Locate every Plasmodium malariae-infected red blood cell.
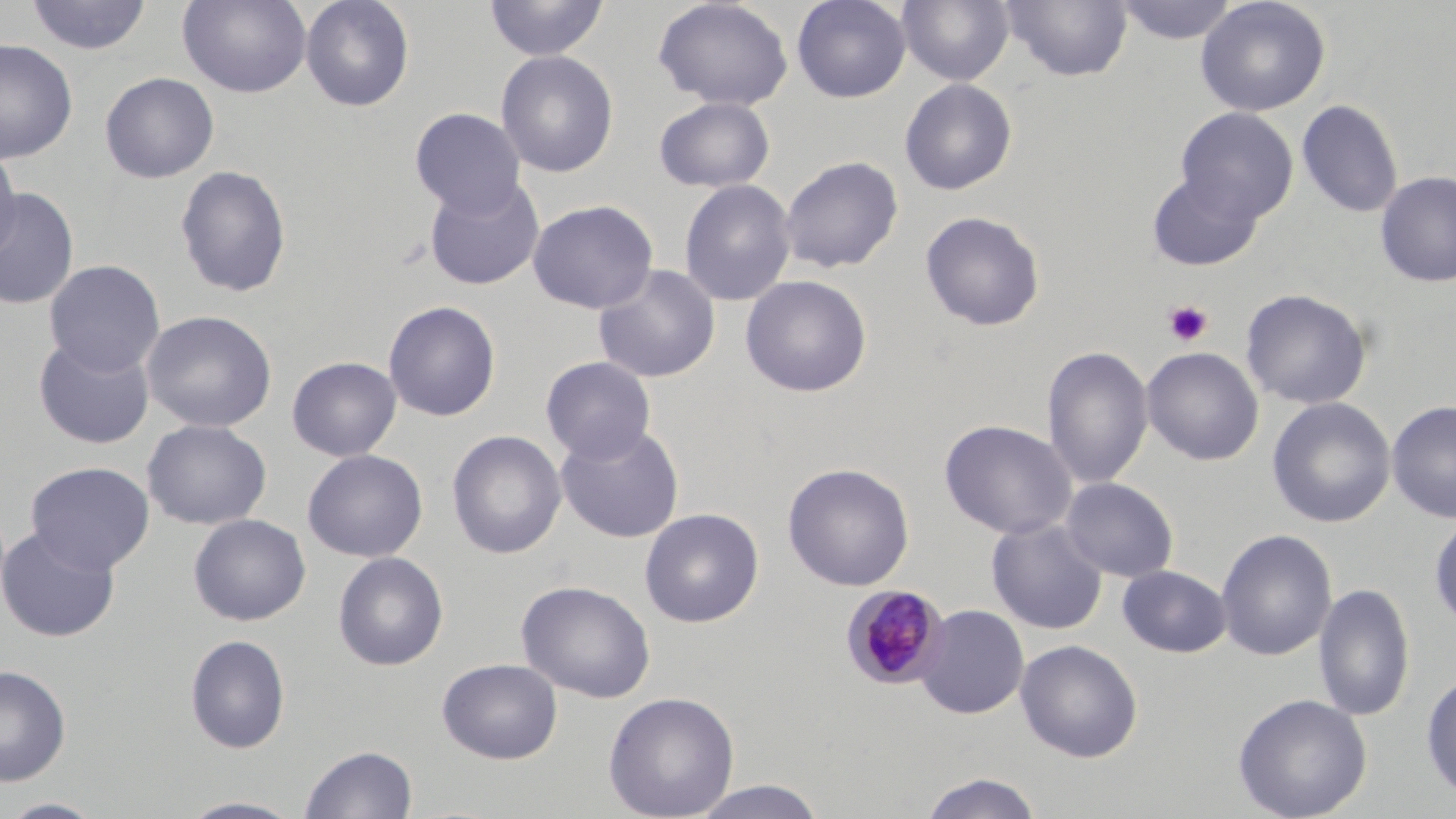

Approximate bounding boxes as (x1, y1, x2, y2) in pixels.
Plasmodium malariae-infected red blood cells: (842, 584, 950, 689).

Summary:
  - Platelet locations: (1163, 299, 1213, 347)
  - Uninfected red blood cell locations: (25, 0, 152, 56), (178, 0, 311, 97), (300, 0, 415, 112), (484, 0, 609, 61), (653, 0, 794, 110), (792, 0, 911, 103), (897, 0, 1014, 86), (1001, 0, 1133, 82), (1113, 0, 1240, 45), (1195, 0, 1331, 117), (0, 40, 78, 163), (496, 50, 619, 178), (100, 72, 219, 183), (899, 78, 1017, 196), (654, 96, 775, 192), (1296, 98, 1403, 218), (410, 107, 526, 217), (1175, 107, 1297, 224), (0, 147, 22, 262), (779, 155, 903, 274), (174, 164, 292, 299), (1146, 171, 1265, 272), (1375, 171, 1456, 287), (423, 175, 545, 290), (679, 179, 797, 306), (0, 188, 79, 310), (528, 199, 658, 314), (920, 211, 1046, 332), (44, 259, 165, 377), (592, 263, 721, 383), (740, 274, 872, 397), (1240, 288, 1372, 409), (383, 300, 501, 422), (141, 310, 277, 433), (33, 334, 155, 450), (1042, 345, 1153, 490), (1142, 346, 1264, 466), (287, 356, 401, 461), (540, 356, 656, 464), (1267, 397, 1395, 528), (1386, 400, 1455, 524), (142, 419, 272, 530), (939, 419, 1076, 540), (556, 423, 684, 543), (447, 430, 567, 560), (302, 448, 428, 563), (25, 461, 155, 574), (782, 462, 914, 591), (1061, 477, 1179, 583), (640, 507, 764, 628), (188, 513, 311, 626), (1429, 513, 1456, 632), (986, 518, 1108, 635), (0, 525, 120, 642), (1215, 528, 1337, 662), (333, 552, 448, 671), (1117, 566, 1232, 657), (516, 580, 656, 703), (1313, 581, 1415, 722), (915, 604, 1028, 719), (185, 634, 291, 754), (1015, 640, 1143, 762), (437, 658, 563, 764), (0, 664, 71, 786), (1421, 669, 1456, 804), (603, 691, 740, 819), (1233, 693, 1372, 818), (300, 744, 418, 819), (917, 772, 1045, 819), (687, 780, 830, 819), (176, 795, 308, 818), (0, 797, 107, 819)
  - Slide-level diagnosis: Plasmodium malariae
  - Preparation: thin blood film
  - Magnification: 1000x
  - Image size: 1456×819 pixels
  - Field of view: one of a larger specimen
  - Stain: May-Grünwald-Giemsa
  - Modality: light microscopy